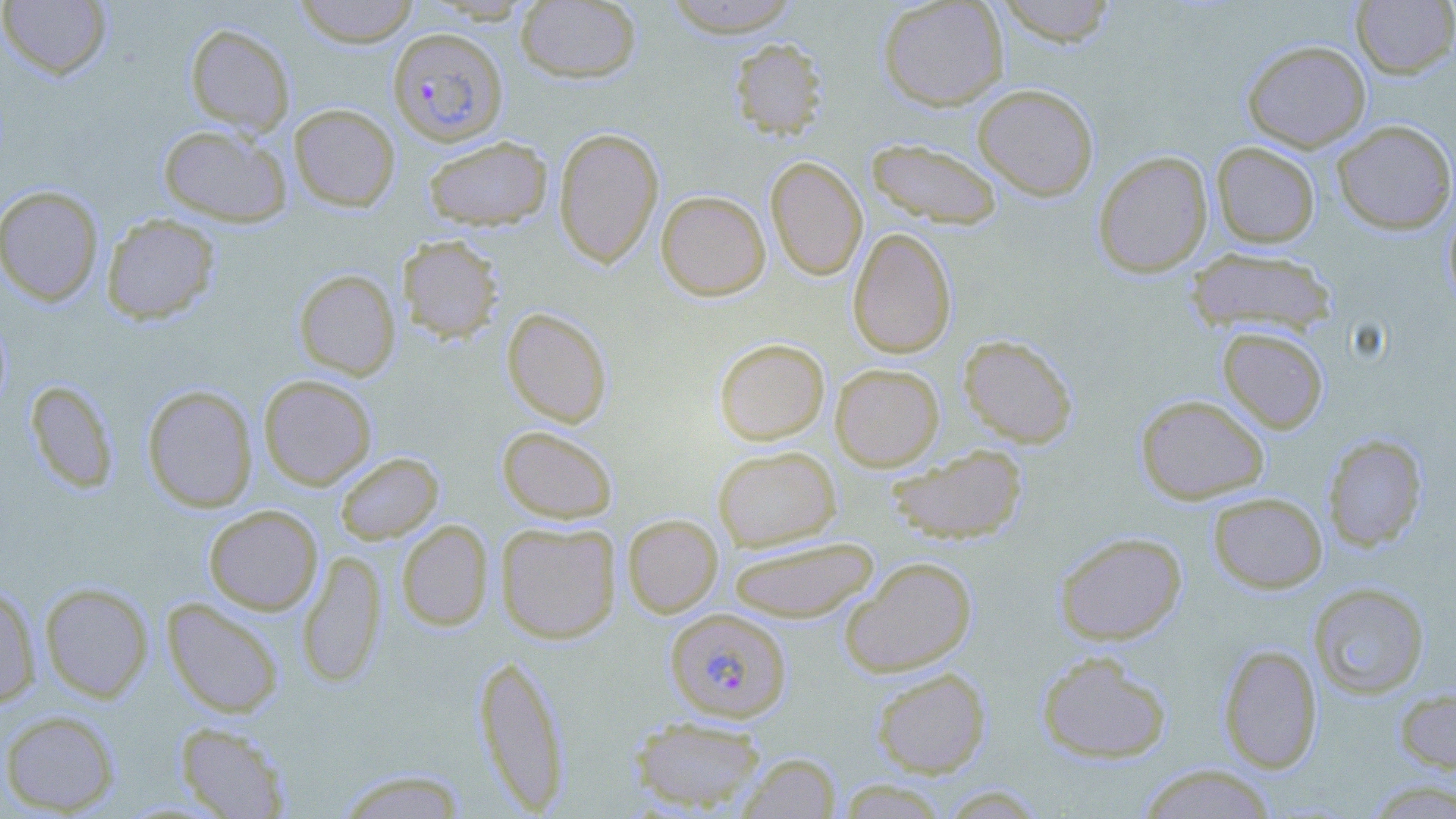

{
  "slide_level_diagnosis": "Plasmodium falciparum",
  "preparation": "thin blood smear",
  "field_of_view": "one of a larger specimen",
  "magnification": "1000x",
  "plasmodium_falciparum_infected_red_blood_cell_locations": "approximate bounding boxes as (x1,y1)-(x2,y2) corner pairs in pixels: (387,26)-(509,146), (666,608)-(791,722)",
  "stain": "May-Grünwald-Giemsa",
  "uninfected_red_blood_cell_locations": "approximate bounding boxes as (x1,y1)-(x2,y2) corner pairs in pixels: (0,0)-(112,80), (293,0)-(421,47), (515,0)-(641,84), (662,0)-(802,37), (878,0)-(1009,110), (995,0)-(1117,46), (1351,0)-(1456,79), (184,22)-(295,136), (730,38)-(827,139), (1242,39)-(1371,152), (973,83)-(1099,201), (289,103)-(400,211), (1332,120)-(1456,234), (158,123)-(292,227), (553,127)-(664,268), (423,136)-(552,231), (866,138)-(1003,229), (1211,142)-(1321,248), (1092,150)-(1213,278), (766,156)-(867,281), (0,185)-(104,306), (656,190)-(770,301), (1444,204)-(1456,313), (101,213)-(220,324), (848,227)-(956,359), (397,234)-(504,343), (1186,247)-(1338,337), (294,269)-(400,380), (502,308)-(612,428), (1217,326)-(1329,434), (958,334)-(1078,448), (714,338)-(830,445), (830,363)-(944,471), (259,374)-(377,490), (25,380)-(119,493), (142,384)-(258,512), (1136,394)-(1270,504), (497,425)-(618,524), (1323,434)-(1427,551), (886,444)-(1028,545), (713,446)-(840,551), (335,452)-(444,544), (1208,492)-(1327,593), (203,504)-(323,615), (622,514)-(723,617), (396,520)-(494,631), (496,521)-(621,643), (1054,531)-(1187,645), (727,537)-(880,622), (297,550)-(386,688), (840,556)-(977,677), (39,582)-(154,703), (1309,582)-(1430,700), (0,585)-(41,709), (162,598)-(285,718), (1218,644)-(1322,773), (473,651)-(571,815), (1036,651)-(1173,764), (871,667)-(990,778), (1394,686)-(1456,778), (1,709)-(121,815), (628,715)-(767,813), (175,722)-(291,818), (737,753)-(841,818), (1137,764)-(1277,818), (333,768)-(471,818), (1362,779)-(1456,818)",
  "image_size": "1456×819 pixels",
  "modality": "light microscopy"
}